Assess the morphology of the red blood cells.
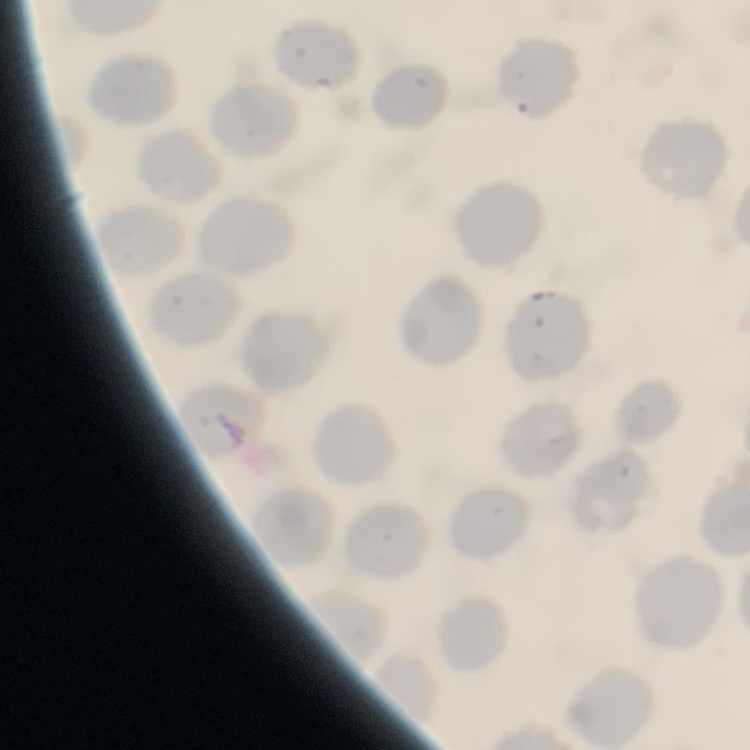

They show no rouleaux formation.

Thin blood smear. Field's or Giemsa stain. Square crop of a larger photomicrograph.